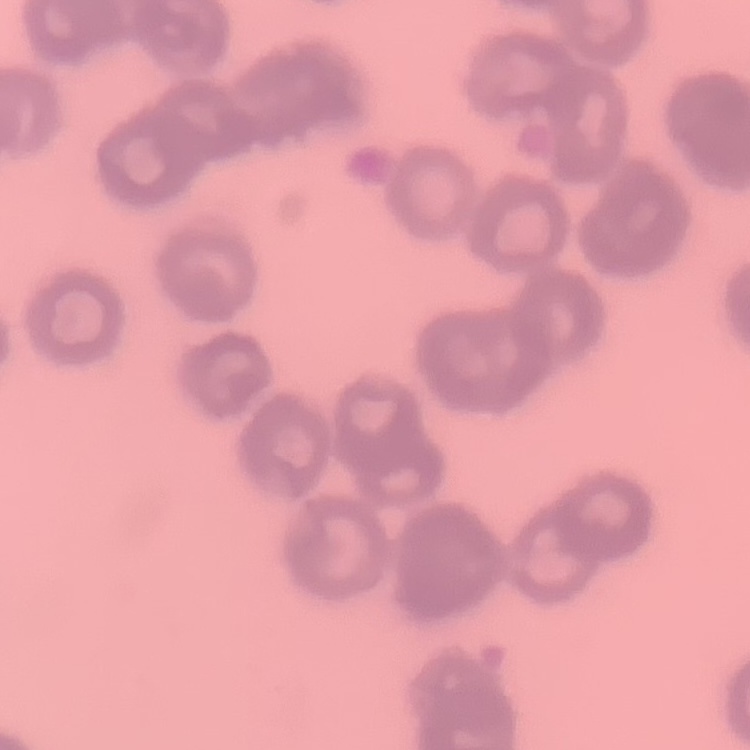
{
  "red_blood_cell_morphology": "rouleaux formation",
  "image_type": "one tile cut from a larger photomicrograph",
  "preparation": "thin blood film",
  "stain": "Field's or Giemsa"
}